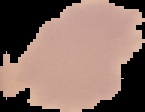

result: no malaria parasites seen
image_type: segmented cell region with the area outside set to black
image_size: 145×112 pixels
preparation: thin blood smear